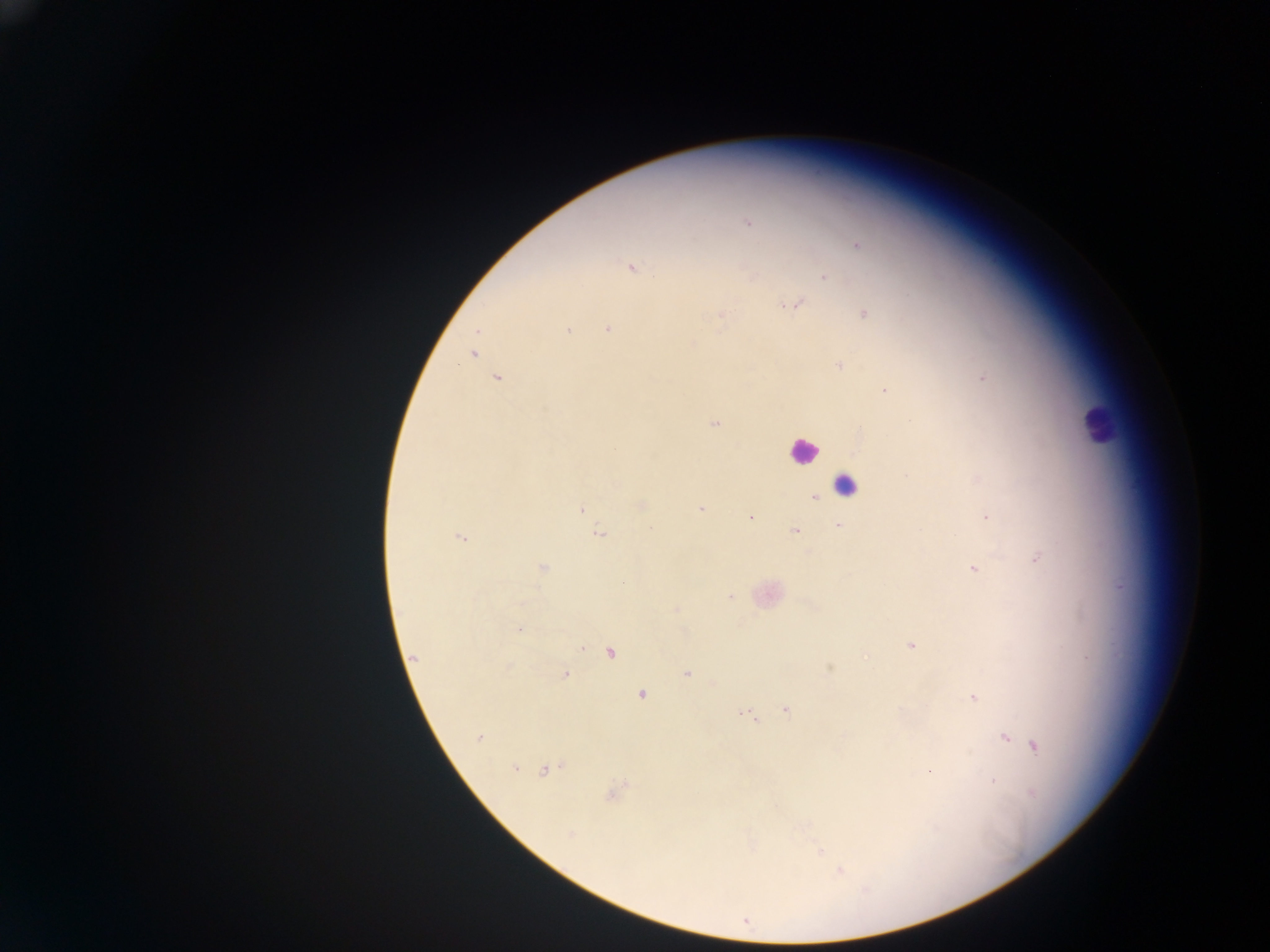
Approximate centers as [x, y] in pixels.
Summary:
  - Leukocyte locations: [1097, 423], [803, 450], [845, 486]
  - Malaria parasite locations: [748, 224], [857, 245], [631, 266], [824, 277], [795, 304], [863, 313], [720, 315], [607, 328], [567, 329], [477, 331], [472, 352], [839, 365], [982, 376], [498, 378], [884, 391], [714, 423], [815, 498], [641, 505], [582, 509], [701, 509], [750, 517], [987, 518], [838, 527], [795, 530], [599, 533], [460, 537], [1037, 558], [973, 567], [542, 568], [729, 597], [675, 610], [519, 629], [911, 645], [581, 646], [610, 652], [413, 658], [830, 668], [564, 674], [687, 674], [641, 694], [973, 697], [785, 709], [748, 712], [478, 737], [1005, 737], [1034, 746], [514, 767], [547, 769], [993, 780], [613, 792], [819, 851], [838, 870]
  - Country: Ghana
  - Preparation: thick blood smear
  - Capture: mobile-phone photograph through a microscope
  - Field of view: single
  - Image size: 1270×952 pixels